Report the malaria status.
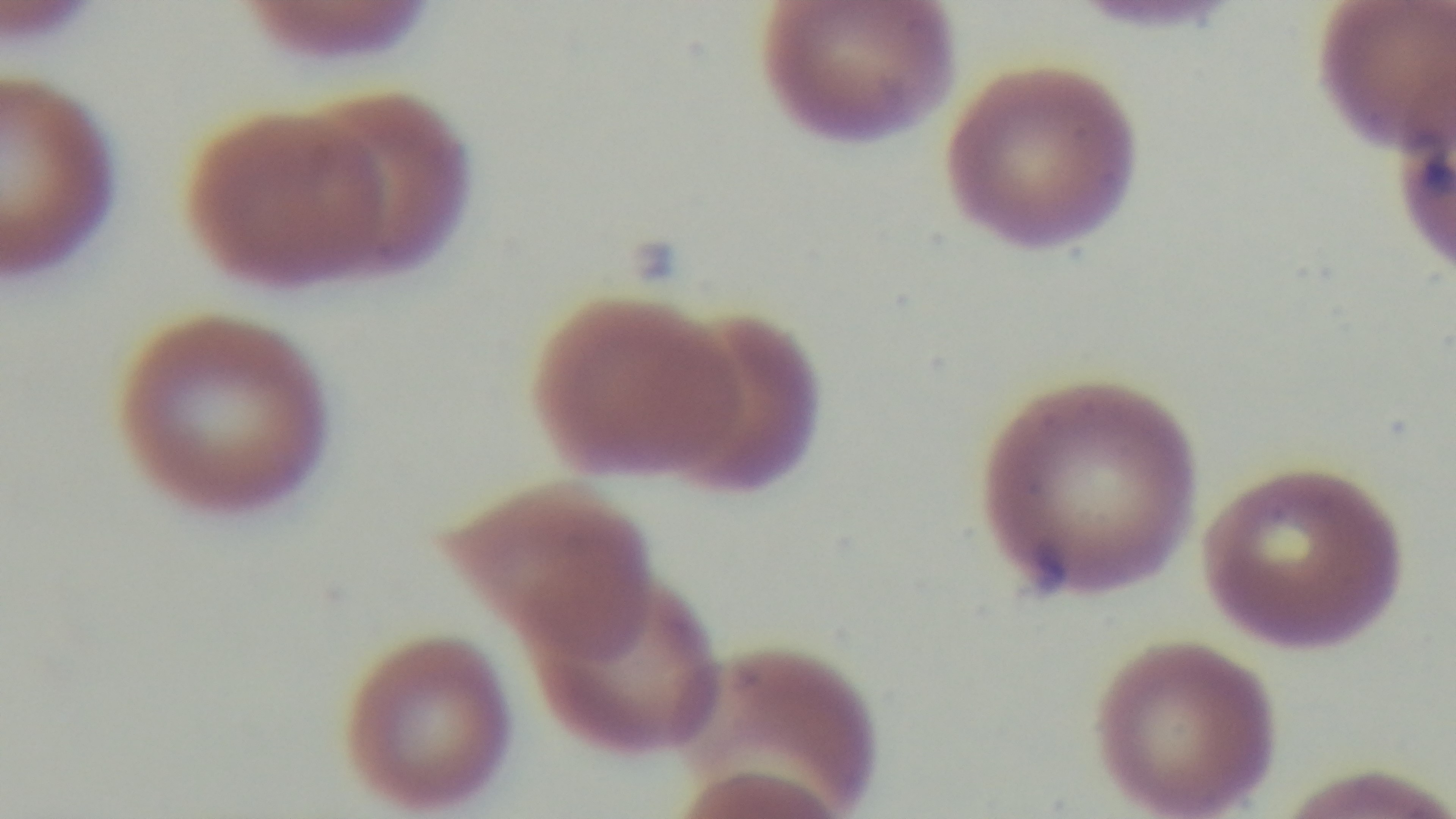
Infected.

Oil-immersion objective, 100x. Captured with a mounted 4K digital camera. Giemsa-stained. Single field of view. Light microscopy. Preparation: thin blood film.